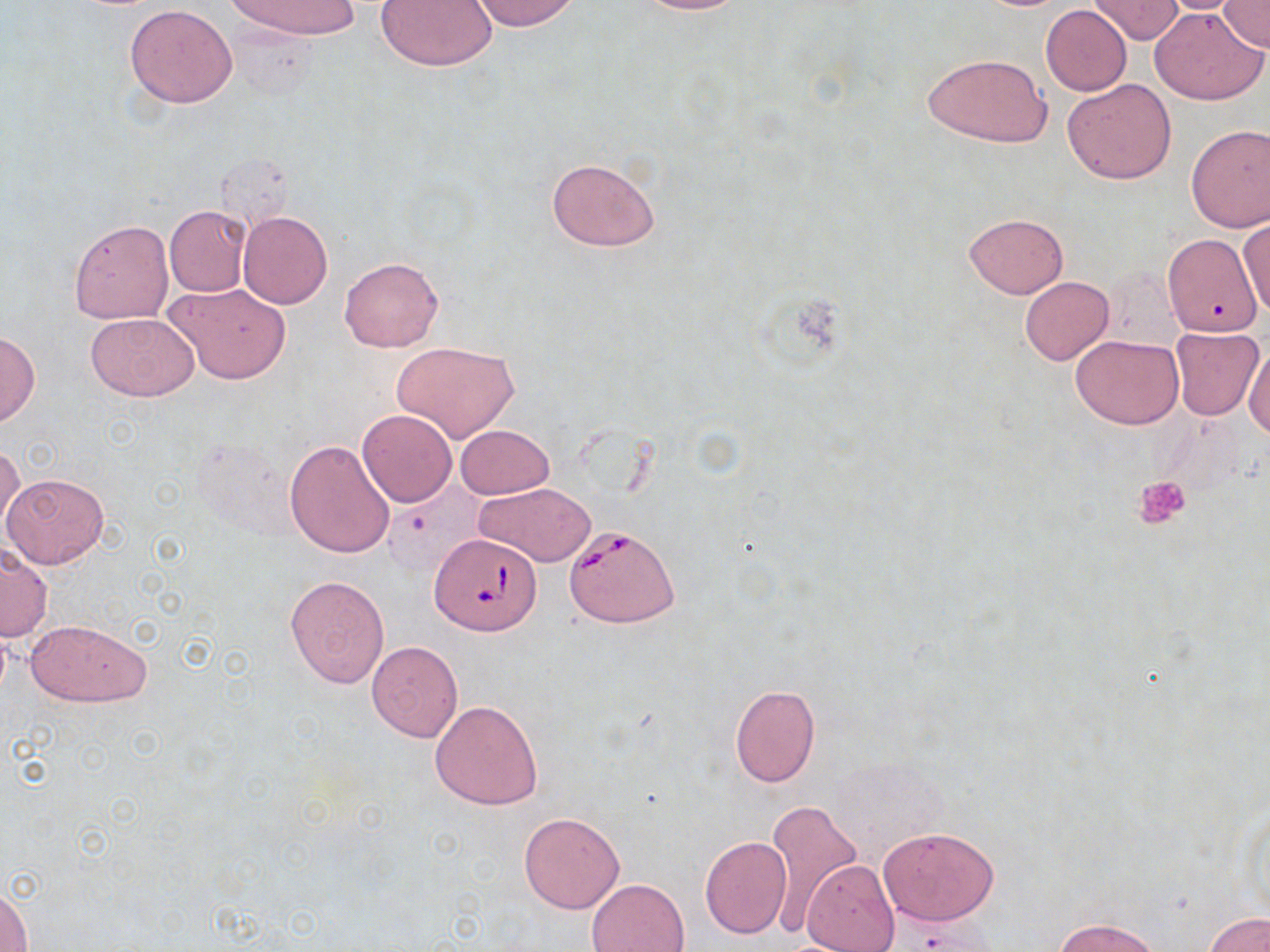

Approximate bounding boxes as (x1, y1, x2, y2) in pixels. Platelet locations: (1133, 475, 1192, 529). Uninfected red blood cell locations: (228, 0, 359, 41), (470, 0, 580, 32), (630, 0, 751, 15), (1149, 0, 1252, 14), (1216, 0, 1270, 52), (376, 1, 497, 71), (1088, 1, 1183, 44), (124, 4, 238, 108), (1040, 5, 1131, 95), (1150, 5, 1269, 106), (921, 51, 1053, 148), (1062, 78, 1177, 186), (1185, 124, 1270, 232), (546, 156, 661, 251), (164, 206, 250, 297), (238, 212, 332, 309), (964, 213, 1068, 298), (1238, 219, 1270, 320), (68, 220, 172, 324), (1163, 235, 1260, 339), (339, 256, 443, 351), (1020, 276, 1113, 364), (161, 282, 291, 385), (86, 312, 198, 401), (1169, 327, 1264, 421), (0, 330, 40, 427), (1071, 335, 1184, 428), (391, 340, 519, 443), (1244, 341, 1270, 440), (357, 408, 457, 508), (456, 424, 553, 500), (285, 439, 397, 559), (1, 444, 23, 535), (2, 472, 110, 568), (474, 482, 596, 566), (1, 544, 53, 641), (285, 575, 390, 687), (25, 618, 151, 707), (366, 642, 463, 743), (729, 684, 819, 787), (430, 700, 542, 810), (763, 799, 865, 932), (518, 811, 625, 913), (878, 826, 1000, 926), (700, 836, 792, 939), (801, 860, 900, 951), (586, 878, 690, 952), (1, 882, 32, 952), (1204, 912, 1270, 952), (1053, 916, 1164, 952). Babesia divergens-infected red blood cell locations: (565, 523, 678, 627), (430, 531, 542, 637). Slide-level diagnosis: Babesia divergens. Image is 1270×952 pixels. One field of a larger specimen. May-Grünwald-Giemsa stain. Captured at 1000x magnification. Thin blood film. Light microscopy.